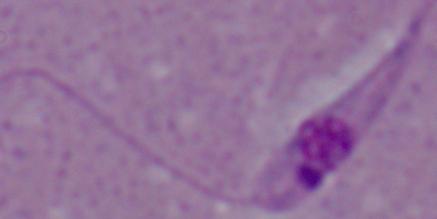
magnification = 1000x
modality = micrograph
identification = Leishmania